Report the malaria status of this cell.
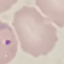

Parasitized.

Giemsa-stained preparation. Photographed with a smartphone camera at the microscope eyepiece. Thin smear of blood. Cell patch, automatically extracted from a larger field of view and resized to 64 × 64 pixels.